Name the blood parasite species.
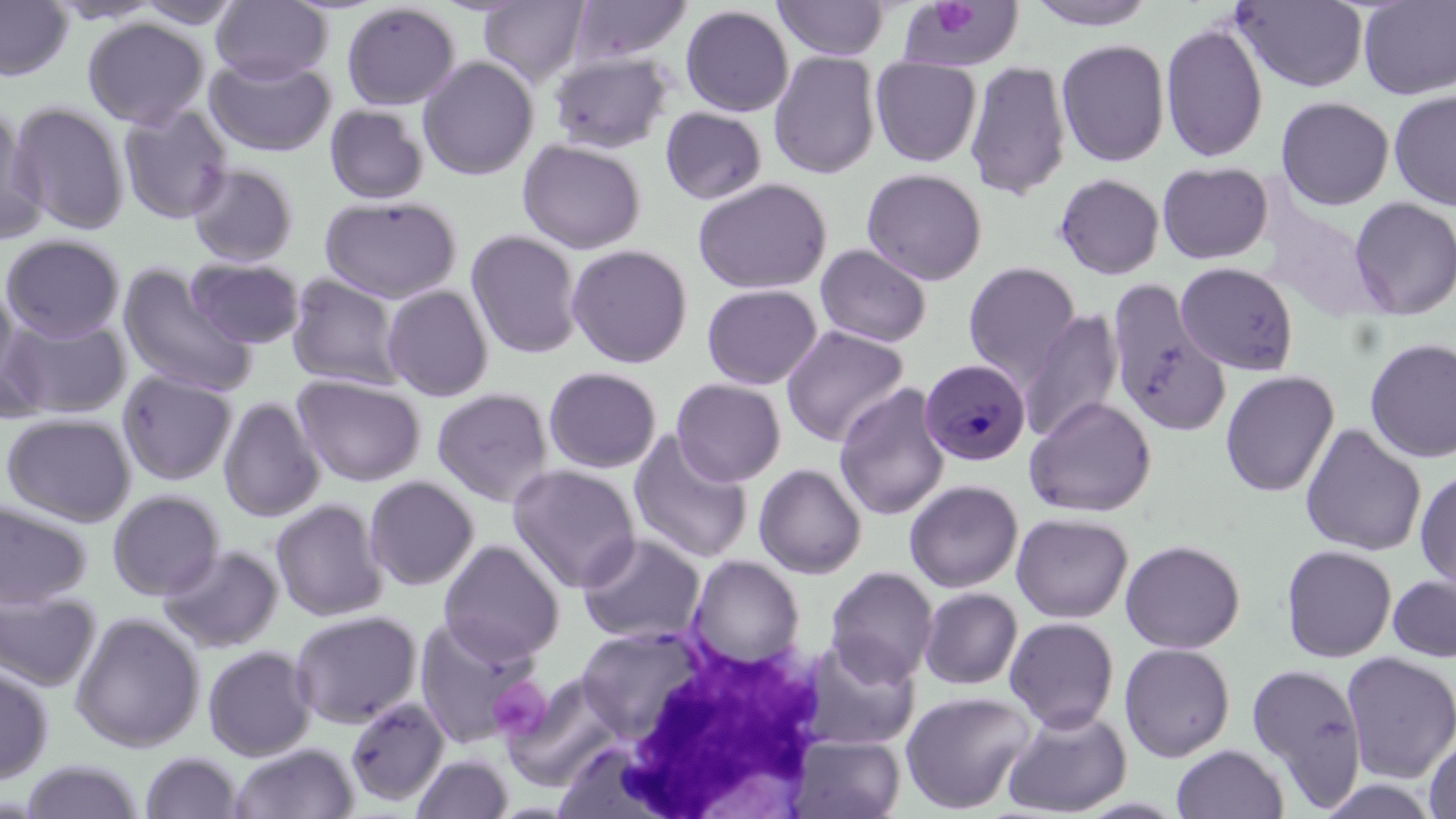

Plasmodium malariae.

image size = 1456×819 pixels
stain = May-Grünwald-Giemsa
uninfected red blood cell locations = approximate bounding boxes as [x1, y1, x2, y2] in pixels: [211, 0, 331, 84], [773, 0, 890, 61], [1026, 0, 1158, 30], [1231, 0, 1369, 92], [0, 1, 74, 81], [132, 1, 247, 30], [478, 1, 590, 88], [568, 1, 693, 65], [1357, 1, 1456, 99], [340, 2, 461, 111], [903, 3, 1022, 73], [679, 4, 794, 117], [82, 17, 210, 129], [1160, 21, 1269, 163], [1056, 38, 1170, 167], [768, 51, 881, 180], [547, 52, 675, 154], [204, 53, 337, 157], [417, 55, 539, 181], [870, 57, 982, 167], [965, 60, 1072, 201], [1389, 89, 1456, 212], [1275, 96, 1394, 210], [8, 101, 130, 235], [117, 104, 234, 225], [325, 104, 430, 205], [0, 107, 49, 247], [660, 107, 768, 205], [517, 138, 647, 254], [1157, 161, 1273, 264], [186, 162, 300, 268], [861, 168, 987, 285], [1054, 173, 1165, 279], [693, 177, 833, 295], [319, 195, 462, 303], [1349, 197, 1456, 320], [465, 229, 584, 360], [0, 234, 125, 342], [566, 243, 694, 368], [814, 243, 932, 348], [186, 257, 306, 349], [963, 261, 1081, 387], [1175, 262, 1297, 374], [118, 264, 257, 398], [286, 273, 406, 392], [1, 279, 22, 404], [1106, 280, 1230, 437], [702, 283, 823, 390], [382, 284, 494, 402], [1020, 309, 1124, 444], [1, 315, 132, 420], [780, 326, 909, 447], [1364, 337, 1456, 463], [543, 366, 663, 473], [116, 369, 237, 487], [1220, 370, 1339, 497], [292, 373, 427, 487], [670, 378, 787, 486], [833, 382, 951, 521], [431, 387, 554, 508], [1023, 395, 1157, 518], [218, 396, 325, 522], [1, 412, 137, 527], [1300, 423, 1426, 557], [629, 430, 753, 564], [507, 463, 642, 593], [753, 463, 867, 579], [1414, 468, 1456, 593], [363, 475, 480, 591], [904, 480, 1023, 593], [106, 489, 226, 601], [0, 498, 93, 609], [270, 499, 388, 621], [1011, 512, 1133, 623], [576, 533, 706, 645], [439, 539, 565, 664], [1120, 539, 1245, 654], [158, 543, 284, 653], [1280, 544, 1397, 663], [687, 555, 806, 669], [825, 565, 940, 685], [1387, 573, 1456, 663], [0, 586, 101, 692], [919, 587, 1023, 690], [289, 609, 423, 729], [70, 612, 205, 752], [413, 614, 543, 748], [1005, 617, 1119, 732], [575, 625, 707, 739], [795, 636, 921, 751], [1119, 643, 1235, 762], [202, 644, 317, 761], [1340, 651, 1456, 784], [0, 662, 54, 784], [1245, 662, 1368, 810], [501, 674, 626, 790], [900, 690, 1036, 814], [344, 696, 449, 807], [1002, 706, 1132, 818], [1424, 733, 1456, 819], [786, 734, 906, 818], [228, 742, 359, 819], [1171, 744, 1289, 819], [140, 751, 244, 818], [410, 753, 514, 818], [20, 760, 145, 818]
modality = optical microscopy
white blood cell locations = approximate bounding boxes as [x1, y1, x2, y2] in pixels: [594, 627, 830, 818]
field of view = single
Plasmodium malariae-infected red blood cell locations = approximate bounding boxes as [x1, y1, x2, y2] in pixels: [921, 361, 1033, 469]
platelet locations = approximate bounding boxes as [x1, y1, x2, y2] in pixels: [926, 2, 985, 37], [486, 679, 551, 741]
preparation = thin blood smear
magnification = 1000x